Give the extent of all Babesia divergens-infected red blood cells.
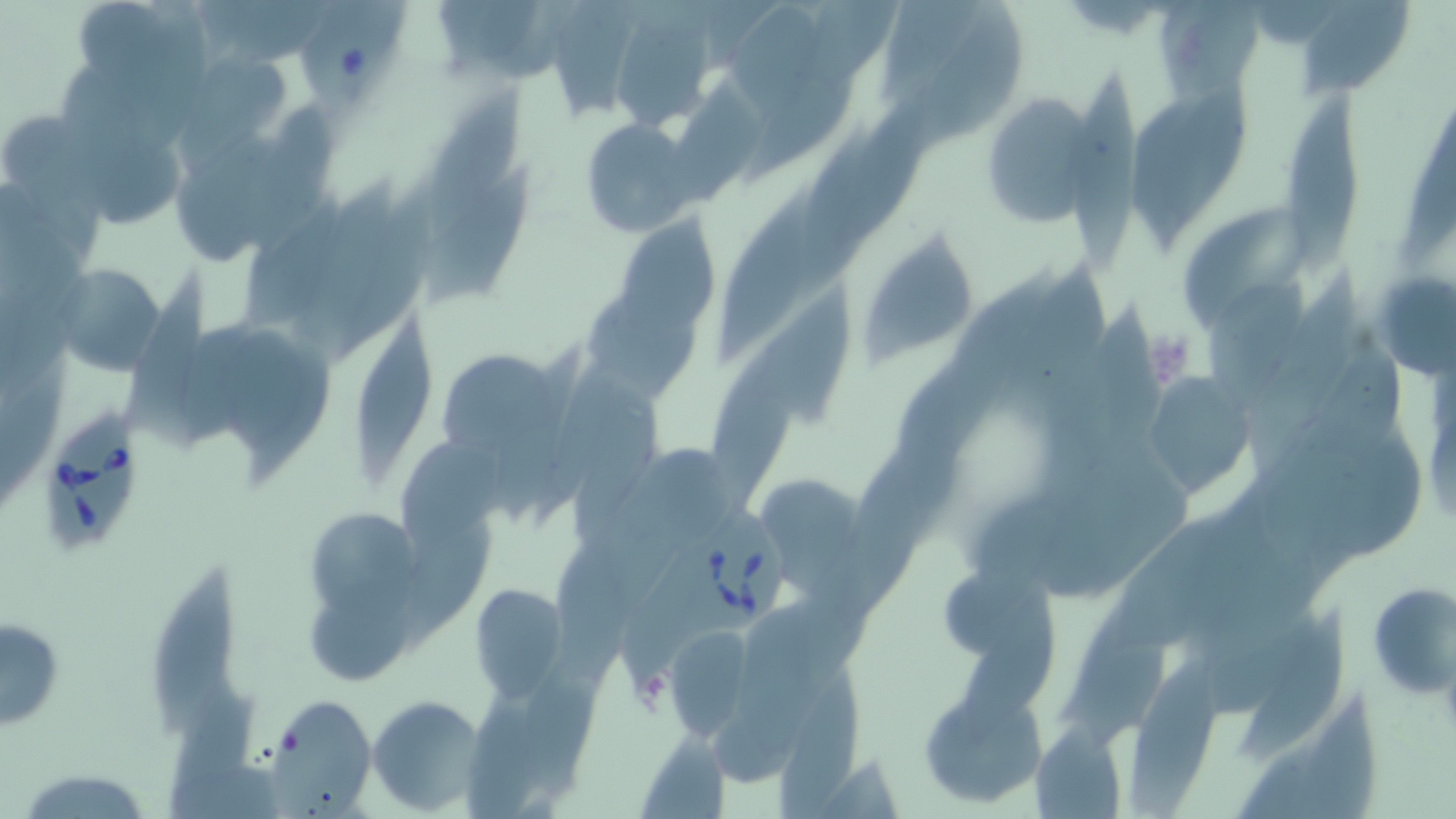

Approximate bounding boxes as (x1, y1, x2, y2) in pixels.
Babesia divergens-infected red blood cells: (32, 388, 151, 560), (662, 489, 793, 646).

slide_level_diagnosis: Babesia divergens
field_of_view: one of a larger specimen
magnification: 1000x
platelet_locations: 'approximate bounding boxes as (x1, y1, x2, y2) in pixels: (1140, 329, 1198, 390), (625, 664, 674, 716)'
stain: May-Grünwald-Giemsa
image_size: 1456×819 pixels
modality: light microscopy
preparation: thin blood film
uninfected_red_blood_cell_locations: 'approximate bounding boxes as (x1, y1, x2, y2) in pixels: (1157, 1, 1264, 105), (1297, 1, 1410, 96), (733, 3, 820, 120), (884, 3, 980, 103), (607, 11, 722, 132), (177, 53, 297, 149), (1070, 74, 1149, 270), (665, 81, 763, 206), (1131, 88, 1253, 235), (422, 89, 527, 240), (980, 92, 1104, 230), (1285, 95, 1366, 278), (579, 120, 697, 235), (425, 165, 539, 304), (289, 187, 397, 360), (722, 192, 816, 360), (1187, 203, 1316, 326), (610, 214, 720, 338), (859, 238, 979, 367), (50, 262, 170, 375), (1001, 263, 1121, 432), (120, 270, 212, 450), (1379, 273, 1455, 379), (1206, 276, 1318, 418), (578, 283, 705, 397), (744, 285, 852, 428), (353, 324, 435, 485), (436, 347, 564, 465), (1140, 374, 1254, 499), (759, 478, 860, 597), (303, 507, 425, 622), (1102, 516, 1239, 660), (943, 563, 1052, 665), (150, 565, 243, 740), (468, 583, 570, 699), (1371, 586, 1456, 699), (303, 591, 416, 685), (1241, 611, 1353, 764), (1, 614, 64, 733), (665, 625, 754, 740), (1130, 660, 1232, 819), (784, 668, 869, 810), (920, 688, 1047, 808), (259, 693, 375, 814), (367, 695, 485, 814), (1029, 723, 1128, 819), (638, 736, 731, 818), (15, 767, 157, 818)'